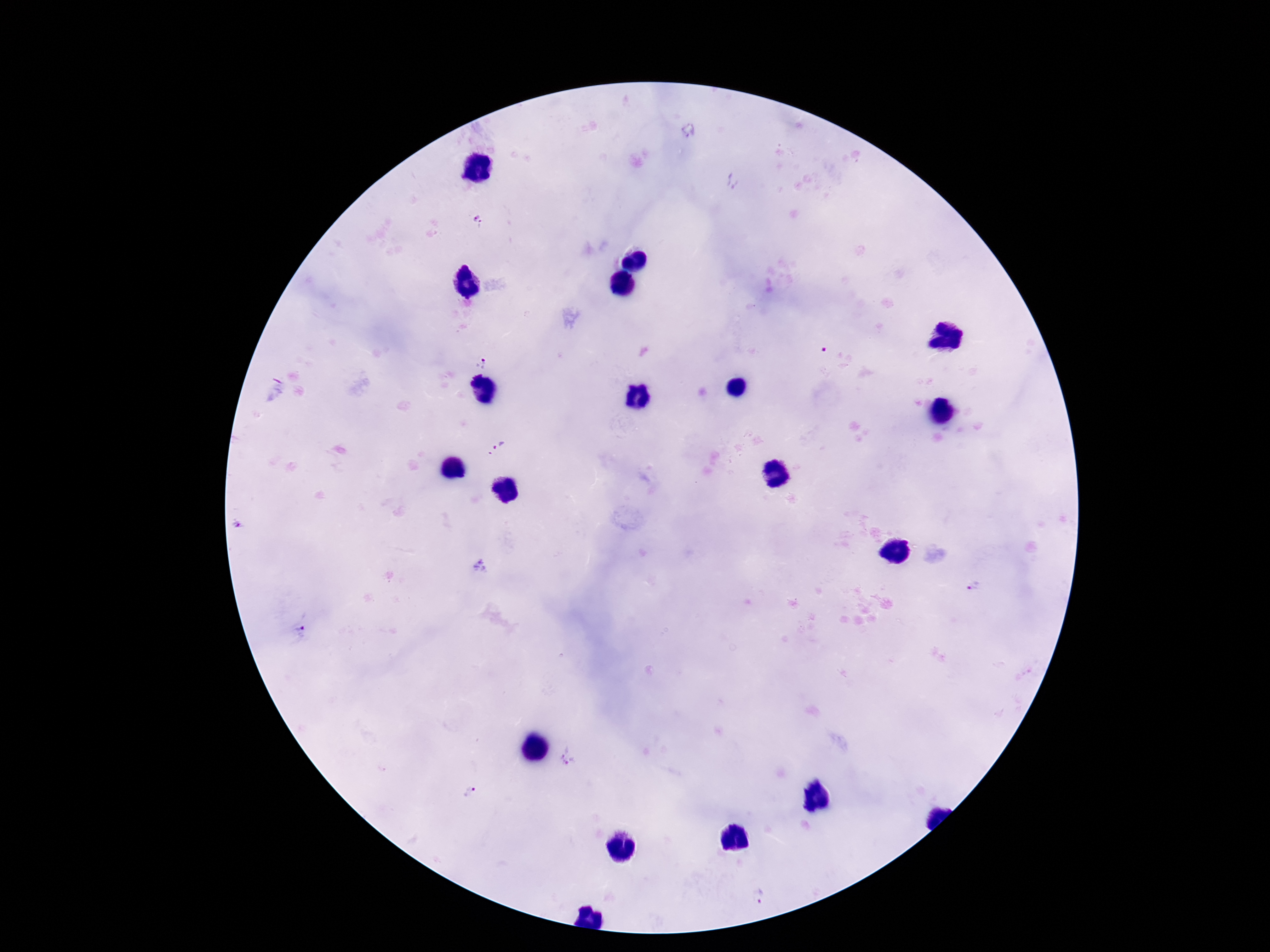

preparation: thick blood smear
magnification: 100x
image_size: 1270×952 pixels
patient_malaria_status: infected
stain: Giemsa
capture: smartphone camera through the microscope eyepiece
plasmodium_parasite_locations: 'approximate centers as [x, y] in pixels: [479, 223], [481, 363], [500, 446], [237, 526], [480, 567], [973, 586], [300, 632], [568, 758], [468, 792], [759, 897]'
field_of_view: one from this slide